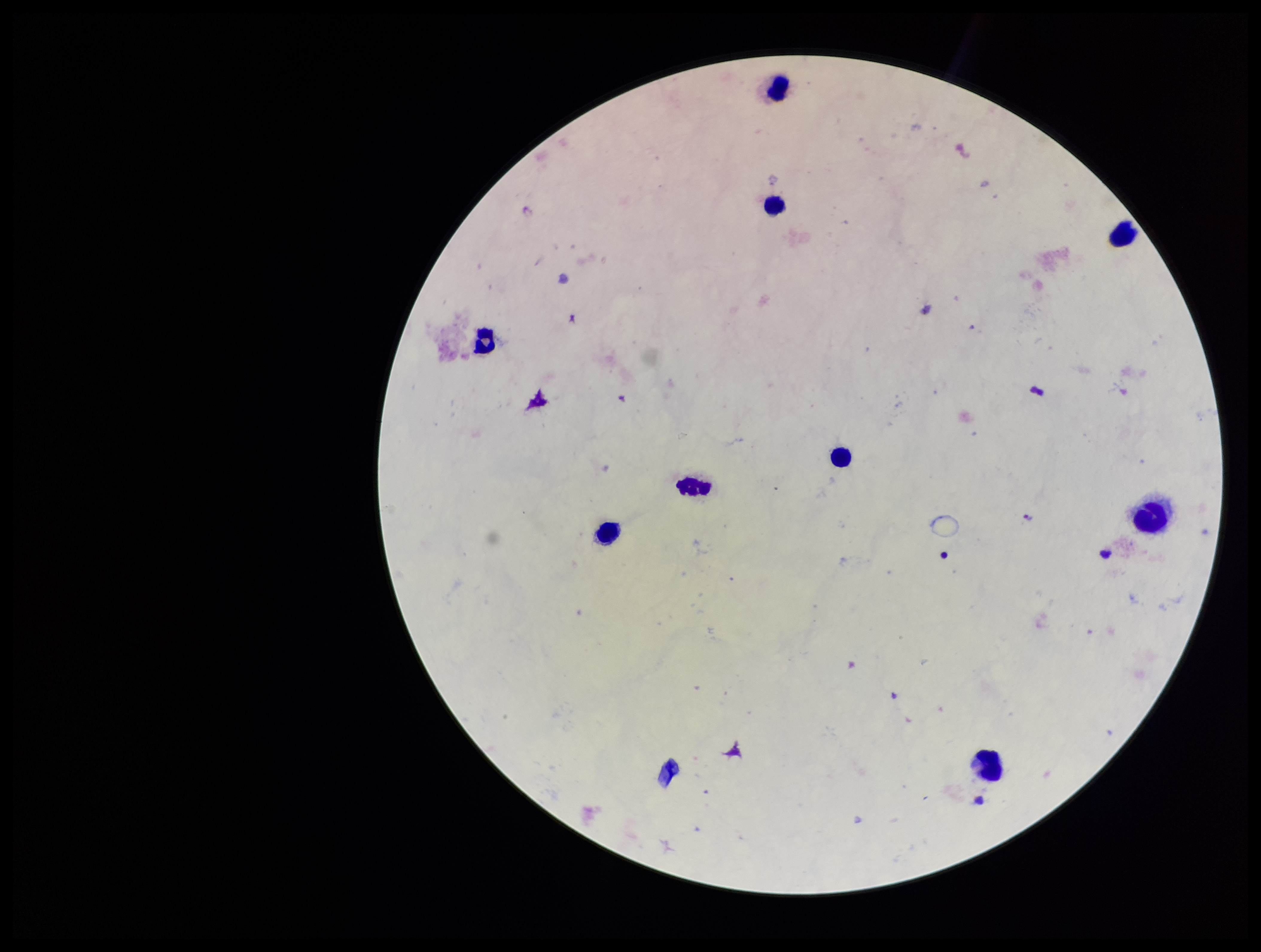

{
  "stain": "Giemsa",
  "field_of_view": "one from this slide",
  "preparation": "thick blood smear",
  "parasite_count": 0,
  "patient_malaria_status": "negative",
  "capture": "smartphone photograph through the microscope eyepiece",
  "plasmodium_parasites": "none seen",
  "image_size": "1261×952 pixels",
  "leukocyte_count": 9
}